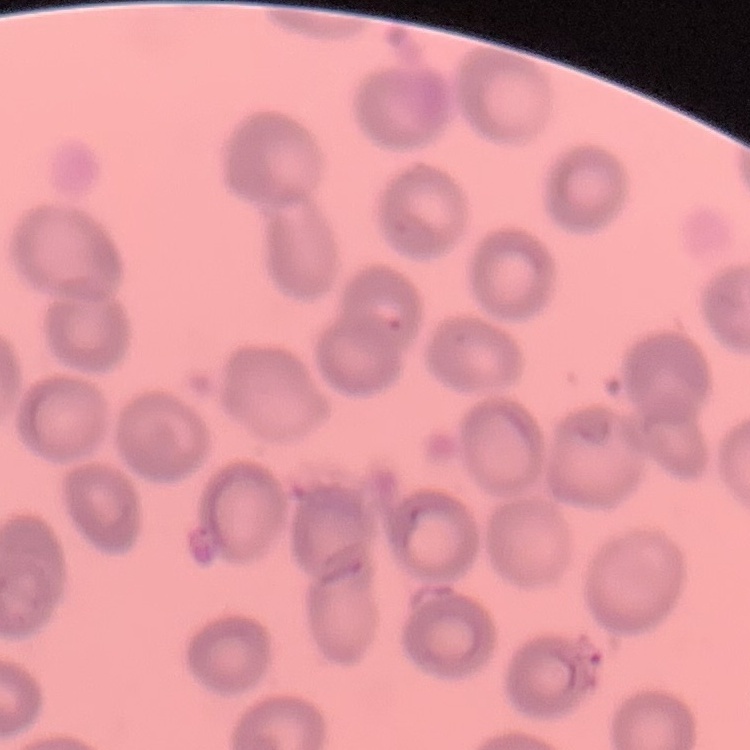

Summary:
  - Erythrocyte morphology: no rouleaux formation
  - Stain: Field's or Giemsa
  - Image type: one tile cut from a larger photomicrograph
  - Preparation: thin blood smear